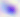

identification = Toxoplasma gondii
magnification = 400x
modality = micrograph